Locate every Plasmodium parasite.
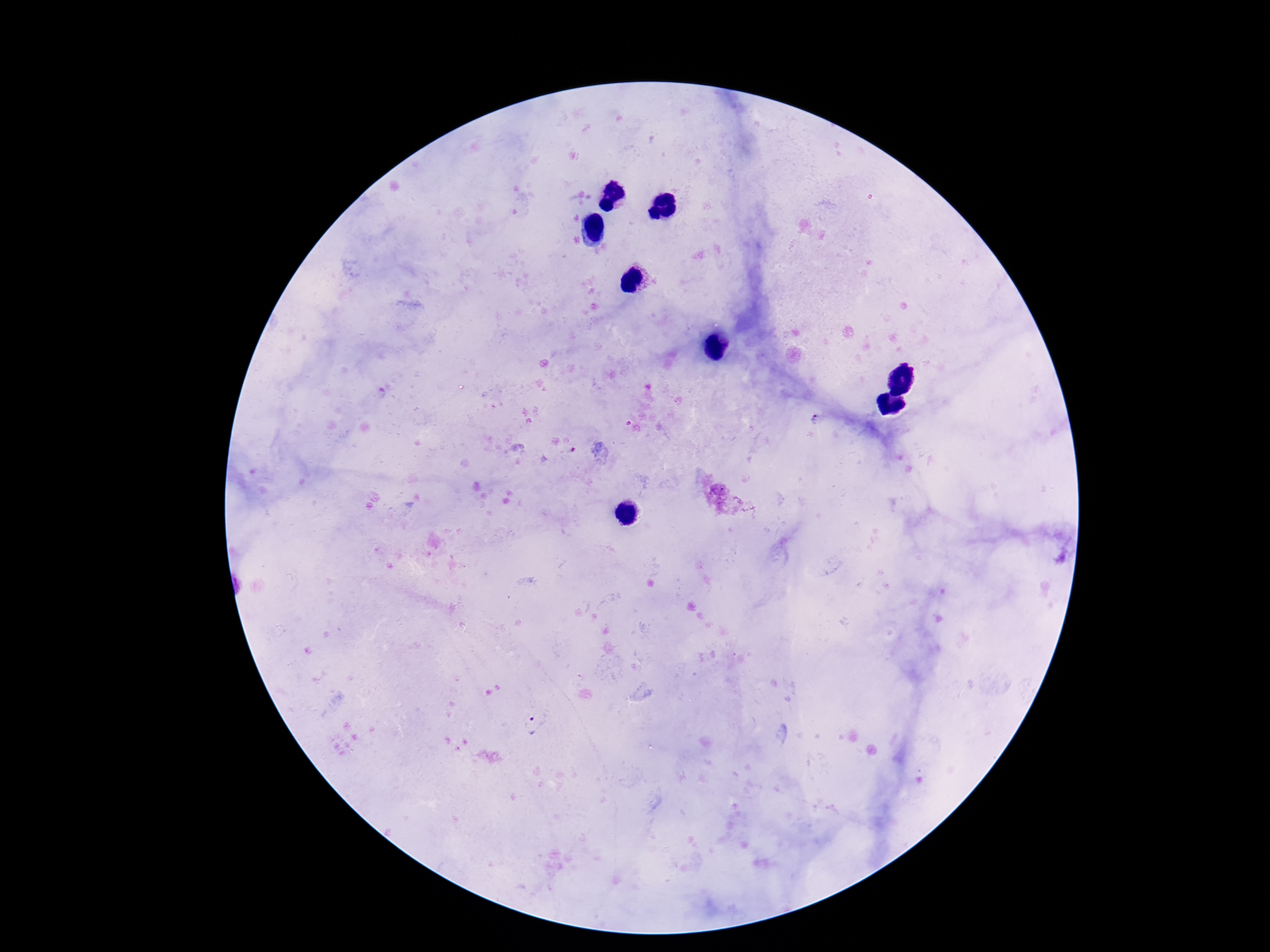

Approximate object centers, in pixels from the top-left corner.
Plasmodium parasites: (x=818, y=420), (x=535, y=726).

100x magnification. Single field of view. Photographed through the microscope eyepiece with a smartphone camera. Giemsa-stained preparation. Image is 1270×952 pixels. Thick blood film. Patient malaria status: infected.